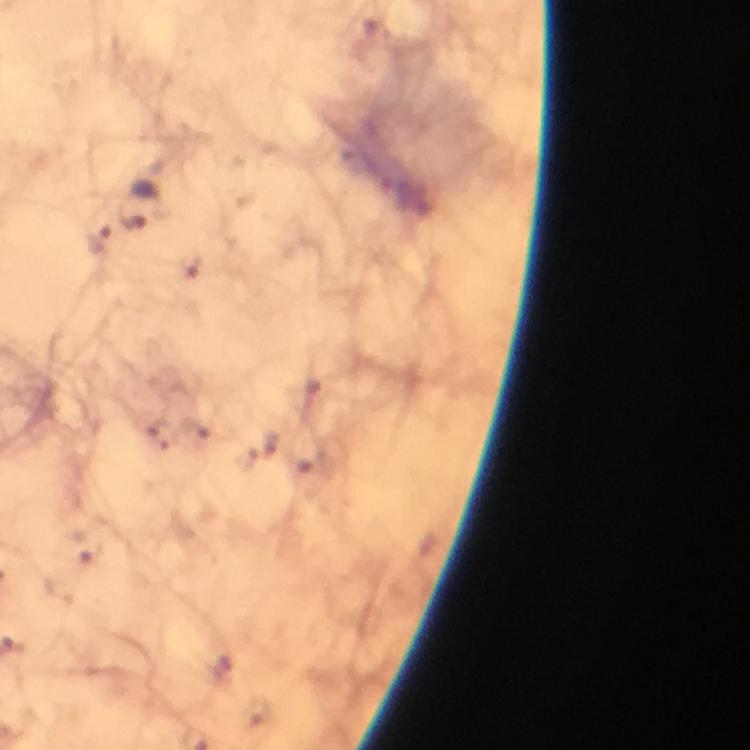
context = from a malaria diagnostic workup
stain = Giemsa
malaria parasite locations = approximate centers as (x, y) in pixels: (134, 218), (98, 241)
immersion oil = used
cropped from = a single field of view
magnification = 100x
preparation = thick smear
capture = smartphone camera through the microscope
image size = 750×750 pixels